State the preparation type.
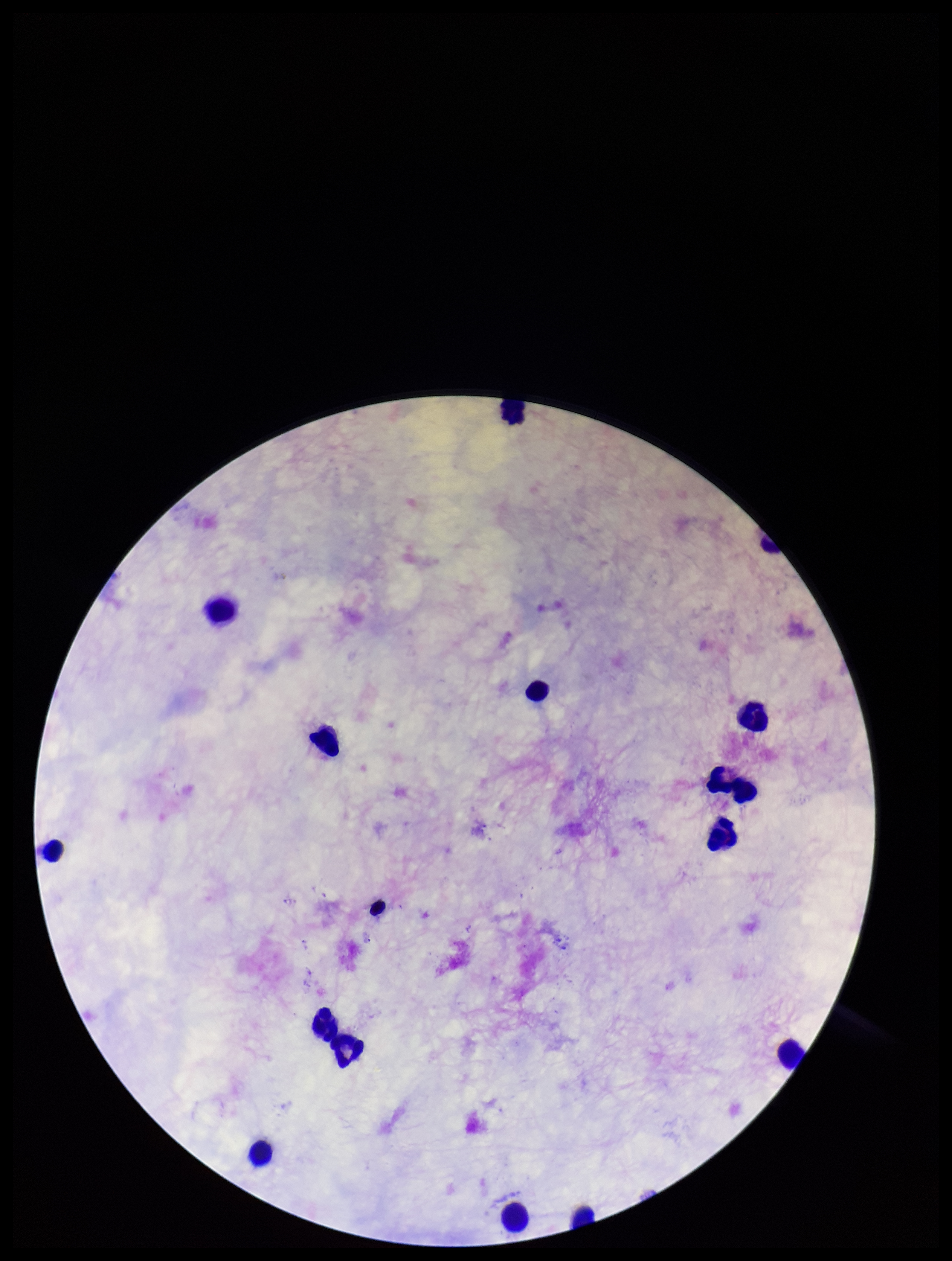

Thick.

Summary:
  - Image size: 952×1261 pixels
  - Leukocyte count: 14
  - Capture: smartphone photograph through the microscope eyepiece
  - Plasmodium parasites: none identified
  - Field of view: one from this slide
  - Stain: Giemsa
  - Patient malaria status: negative
  - Parasite count: 0